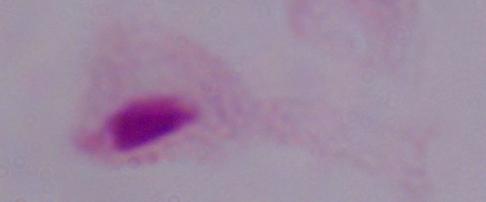

Micrograph. A trichomonad is seen. 1000x magnification.